Classify this cell by malaria status.
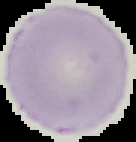
It is uninfected.

{
  "image_size": "136×142 pixels",
  "image_type": "segmented cell region with the area outside set to black",
  "preparation": "thin blood smear"
}